Point out each malaria parasite and each leukocyte.
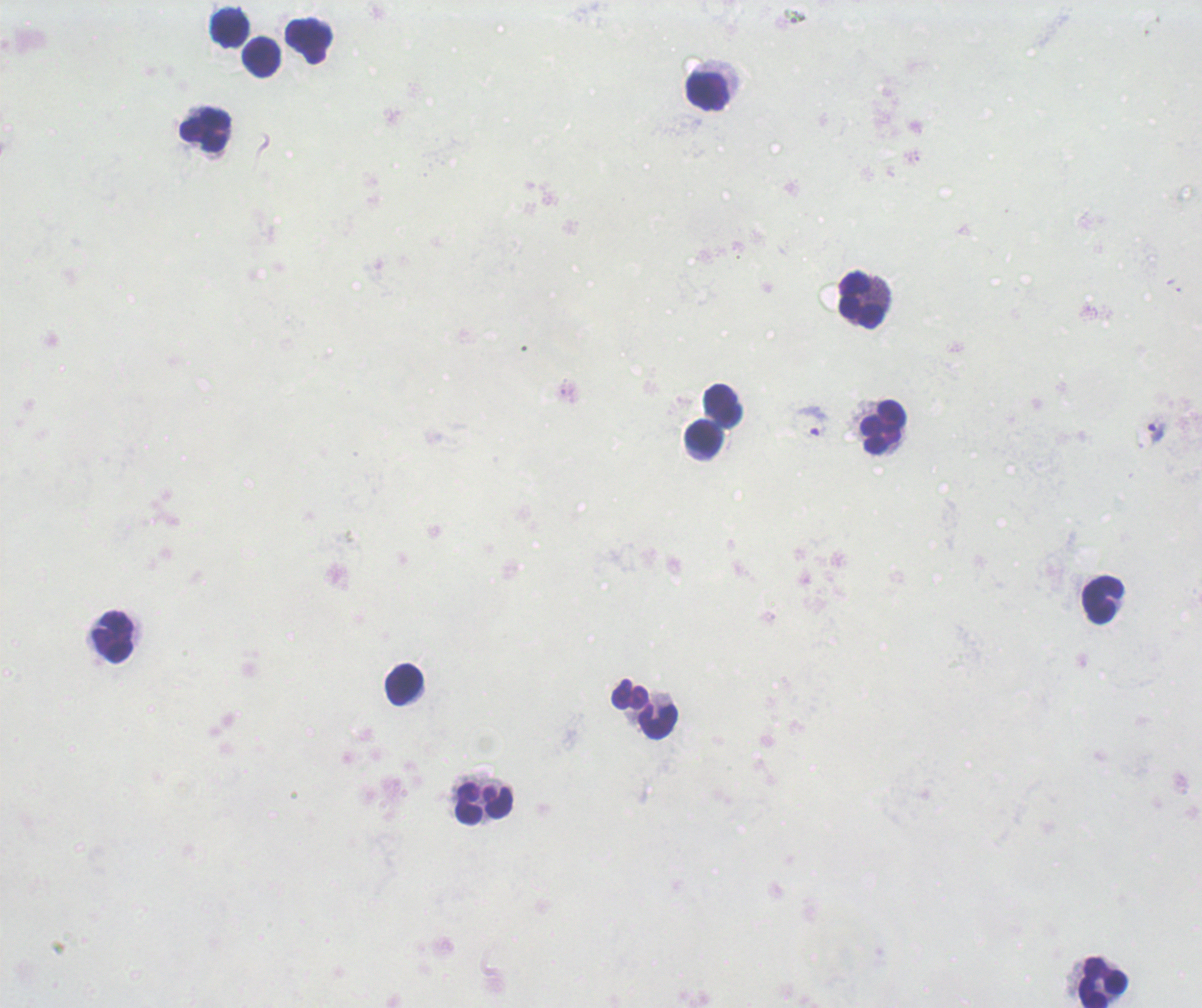
Approximate object centers, in pixels from the top-left corner.
Trophozoites: (x=813, y=421), (x=1156, y=433).
No schizont or gametocyte forms observed.
Leukocytes: (x=230, y=28), (x=309, y=41), (x=261, y=57), (x=706, y=92), (x=205, y=130), (x=863, y=300), (x=722, y=405), (x=882, y=429), (x=703, y=438), (x=1102, y=600), (x=114, y=637), (x=404, y=685), (x=646, y=711), (x=483, y=803), (x=1102, y=982).

Thick smear of blood. Romanowsky stain. Single field of view. Image is 1202×1008 pixels. Previously used in an actual diagnosis. Background quality: unsatisfactory. Captured at 100x magnification.